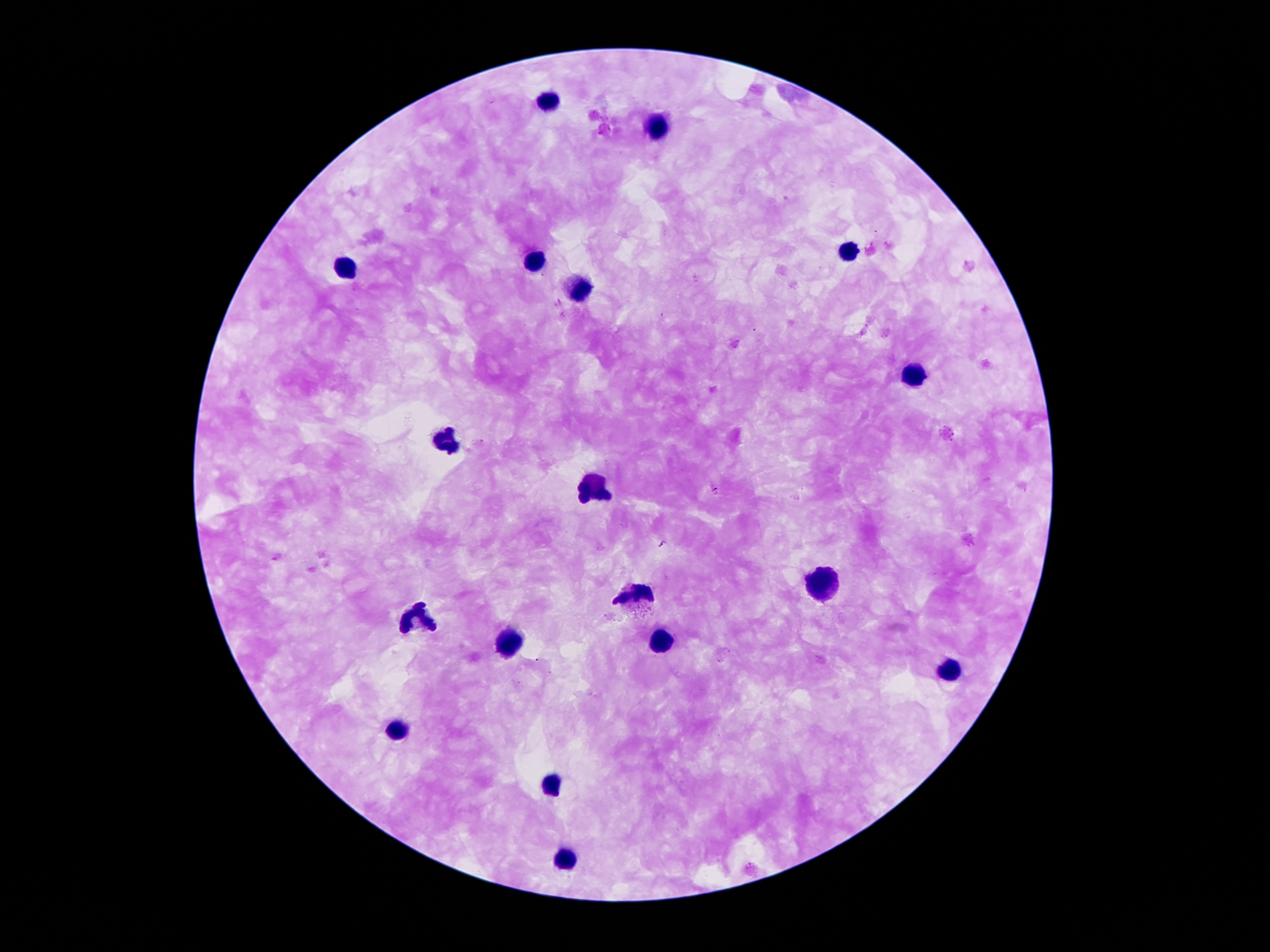
Approximate centers as (x, y) in pixels. Plasmodium parasite locations: (559, 303), (717, 488), (662, 544). Leukocyte locations: (552, 107), (658, 124), (849, 254), (538, 265), (583, 292), (919, 376), (445, 440), (592, 491), (822, 589), (638, 597), (416, 624), (656, 642), (509, 647), (952, 673), (400, 733), (554, 787), (570, 862). Photographed through the microscope eyepiece with a smartphone camera. Patient malaria status: positive for Plasmodium falciparum. Giemsa-stained preparation. 100x magnification. Thick blood smear. Image is 1270×952 pixels. Single field of view.